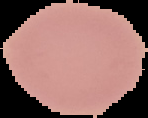

image type = cell region segmented out of the field of view; surrounding area masked to black
image size = 148×118 pixels
preparation = thin blood smear
result = no malaria parasites seen